Give a bounding box for every leukocyte visible.
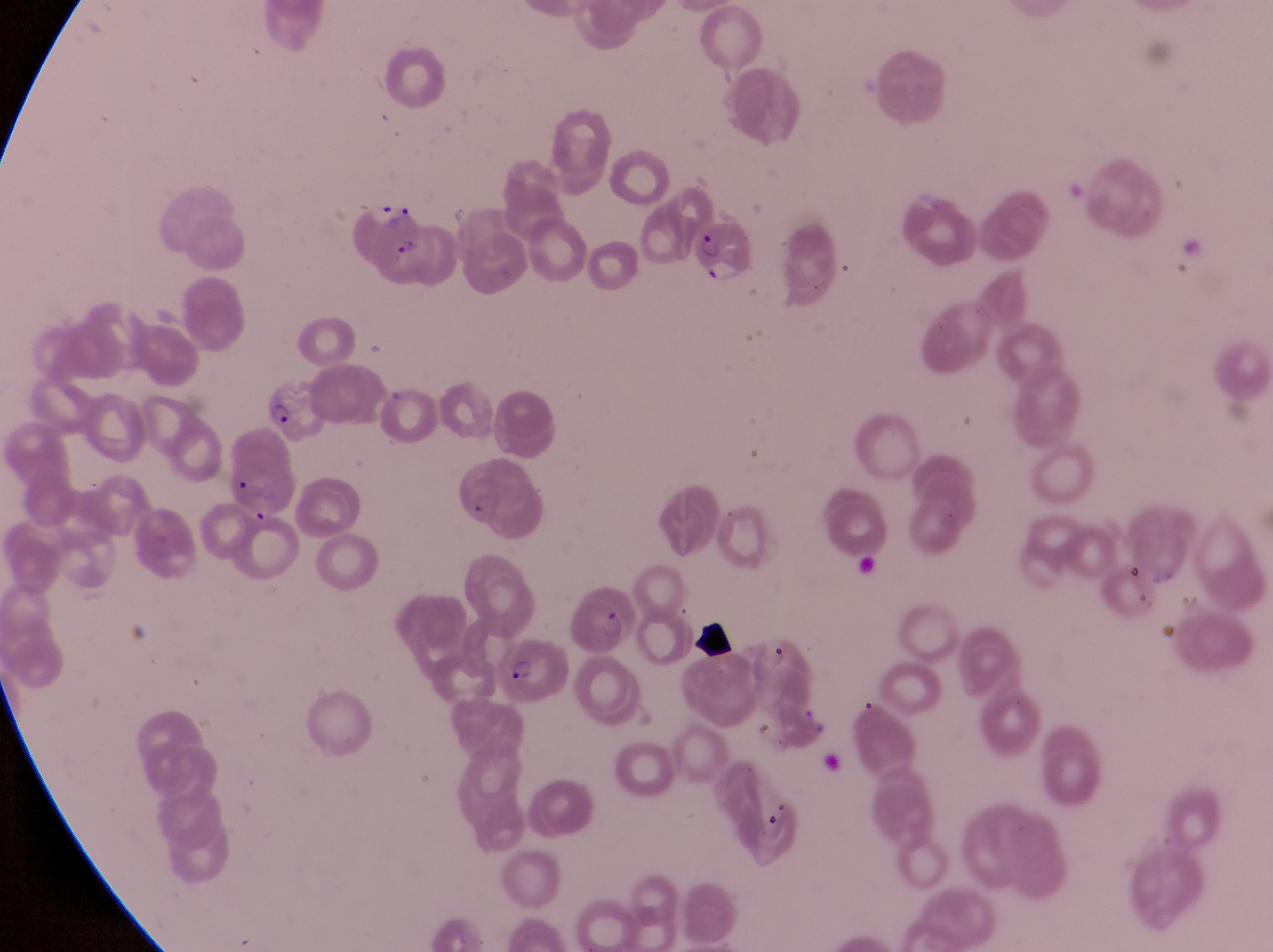

No leukocytes observed.

country = Uganda
parasitised red blood cell locations = approximate bounding boxes as {left, top, right, bottom} in pixels: {352, 199, 434, 281}, {689, 205, 756, 283}, {257, 382, 329, 452}, {222, 439, 291, 519}, {569, 587, 639, 661}, {497, 642, 569, 712}
preparation = thin blood film
magnification = 1000x
capture = smartphone photograph through the eyepiece of an Olympus CX-23 microscope
field of view = single
artifact (platelet-like body, stain precipitate, or debris) locations = approximate bounding boxes as {left, top, right, bottom} in pixels: {694, 619, 746, 659}, {759, 797, 798, 840}
image size = 1273×952 pixels